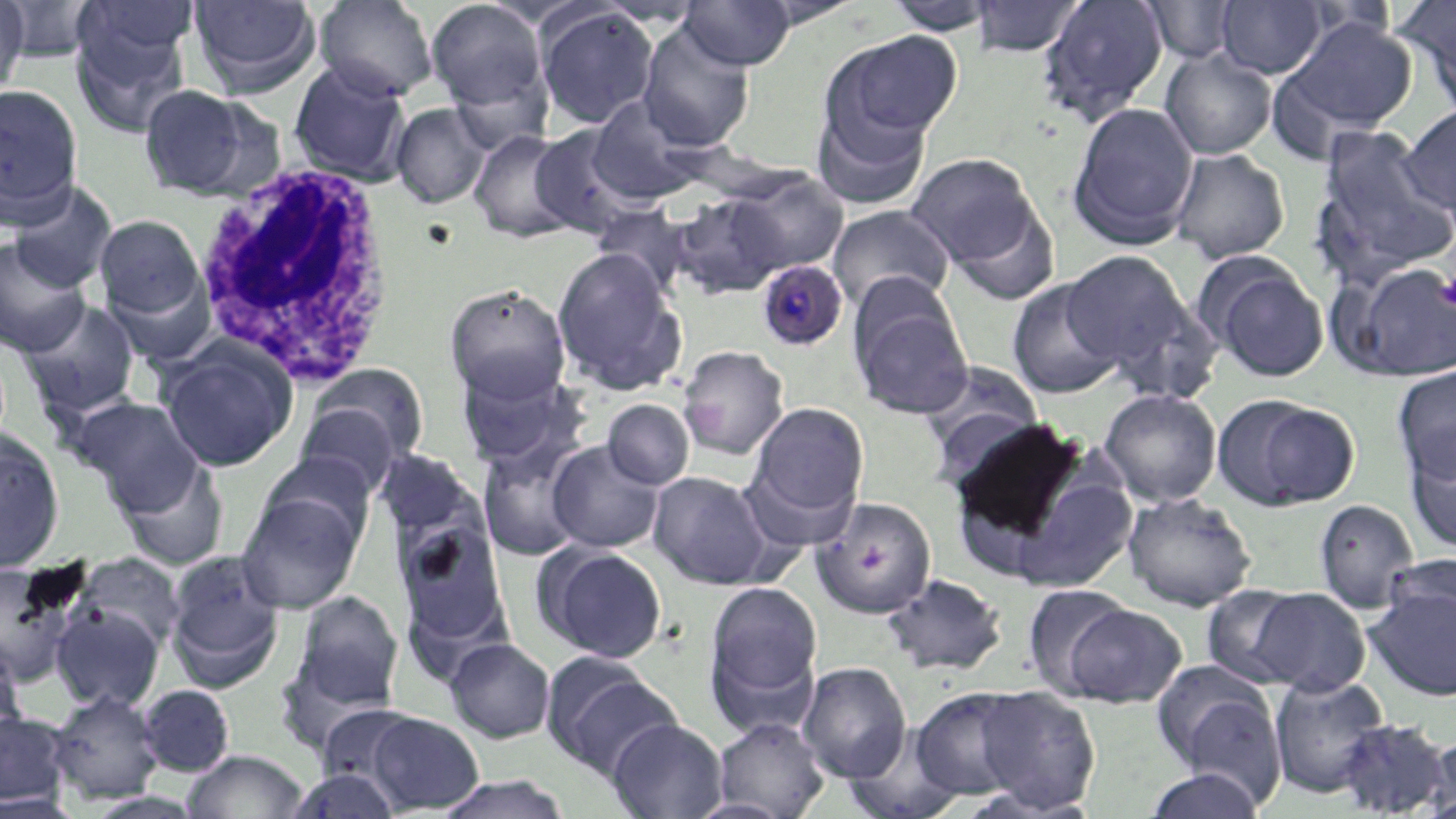

Summary:
  - Coordinate format: approximate bounding boxes as [x1, y1, x2, y2] in pixels
  - Plasmodium malariae-infected red blood cell locations: [757, 261, 848, 351]
  - White blood cell locations: [191, 161, 401, 386]
  - Uninfected red blood cell locations: [0, 0, 31, 105], [187, 0, 322, 98], [313, 0, 440, 101], [425, 0, 550, 114], [966, 0, 1088, 57], [1036, 0, 1169, 125], [2, 1, 106, 63], [73, 1, 201, 75], [678, 1, 797, 70], [745, 1, 866, 29], [883, 1, 999, 35], [1140, 1, 1242, 64], [1215, 1, 1328, 79], [1396, 1, 1456, 108], [533, 4, 661, 129], [69, 15, 193, 137], [1283, 17, 1418, 134], [637, 20, 756, 151], [828, 31, 963, 145], [1160, 50, 1276, 159], [288, 61, 413, 185], [0, 84, 84, 224], [138, 84, 263, 200], [812, 94, 934, 209], [587, 95, 712, 205], [1067, 102, 1200, 249], [390, 103, 492, 209], [1399, 104, 1456, 222], [530, 124, 649, 238], [1311, 124, 1456, 285], [469, 129, 579, 242], [1170, 148, 1290, 263], [905, 153, 1044, 271], [724, 171, 848, 278], [5, 182, 118, 293], [672, 192, 792, 299], [945, 195, 1061, 306], [827, 204, 954, 313], [94, 213, 207, 328], [0, 237, 92, 357], [551, 247, 687, 396], [1059, 250, 1201, 381], [1199, 256, 1330, 382], [1335, 259, 1456, 382], [1005, 277, 1123, 400], [444, 283, 571, 404], [850, 292, 974, 419], [20, 299, 141, 419], [157, 340, 297, 472], [678, 345, 789, 460], [916, 362, 1045, 477], [455, 363, 589, 476], [301, 364, 429, 476], [1392, 365, 1456, 482], [1099, 388, 1222, 506], [1211, 394, 1359, 512], [73, 397, 205, 511], [602, 399, 694, 490], [294, 400, 405, 500], [746, 401, 870, 529], [945, 417, 1099, 570], [0, 432, 65, 573], [1406, 435, 1456, 554], [546, 440, 665, 553], [478, 443, 587, 562], [117, 458, 228, 571], [1008, 468, 1140, 594], [647, 471, 773, 590], [237, 488, 364, 614], [1122, 491, 1256, 611], [810, 497, 939, 618], [1314, 499, 1419, 613], [395, 515, 511, 648], [535, 544, 668, 663], [70, 552, 187, 657], [163, 552, 286, 692], [0, 560, 82, 688], [1363, 568, 1456, 701], [883, 574, 1008, 677], [702, 580, 824, 730], [1200, 584, 1314, 690], [1022, 585, 1138, 699], [1248, 587, 1371, 696], [290, 590, 405, 715], [50, 602, 165, 712], [1058, 603, 1187, 708], [445, 638, 555, 742], [0, 649, 26, 747], [542, 654, 682, 779], [797, 661, 911, 782], [1151, 661, 1285, 801], [1269, 674, 1391, 799], [137, 684, 235, 777], [973, 686, 1101, 814], [910, 687, 1031, 801], [48, 689, 164, 804], [0, 711, 73, 808], [361, 711, 486, 813], [713, 717, 829, 818], [606, 718, 727, 819], [1333, 718, 1452, 817], [842, 727, 963, 819], [1421, 733, 1455, 817], [181, 750, 308, 818], [1141, 767, 1268, 819], [288, 768, 402, 818], [435, 774, 571, 819], [686, 798, 794, 819]
  - Platelet locations: [1437, 274, 1456, 309], [686, 402, 726, 436]
  - Slide-level diagnosis: Plasmodium malariae
  - Stain: May-Grünwald-Giemsa
  - Preparation: thin blood smear
  - Modality: light microscopy
  - Magnification: 1000x
  - Field of view: one of a larger specimen
  - Image size: 1456×819 pixels